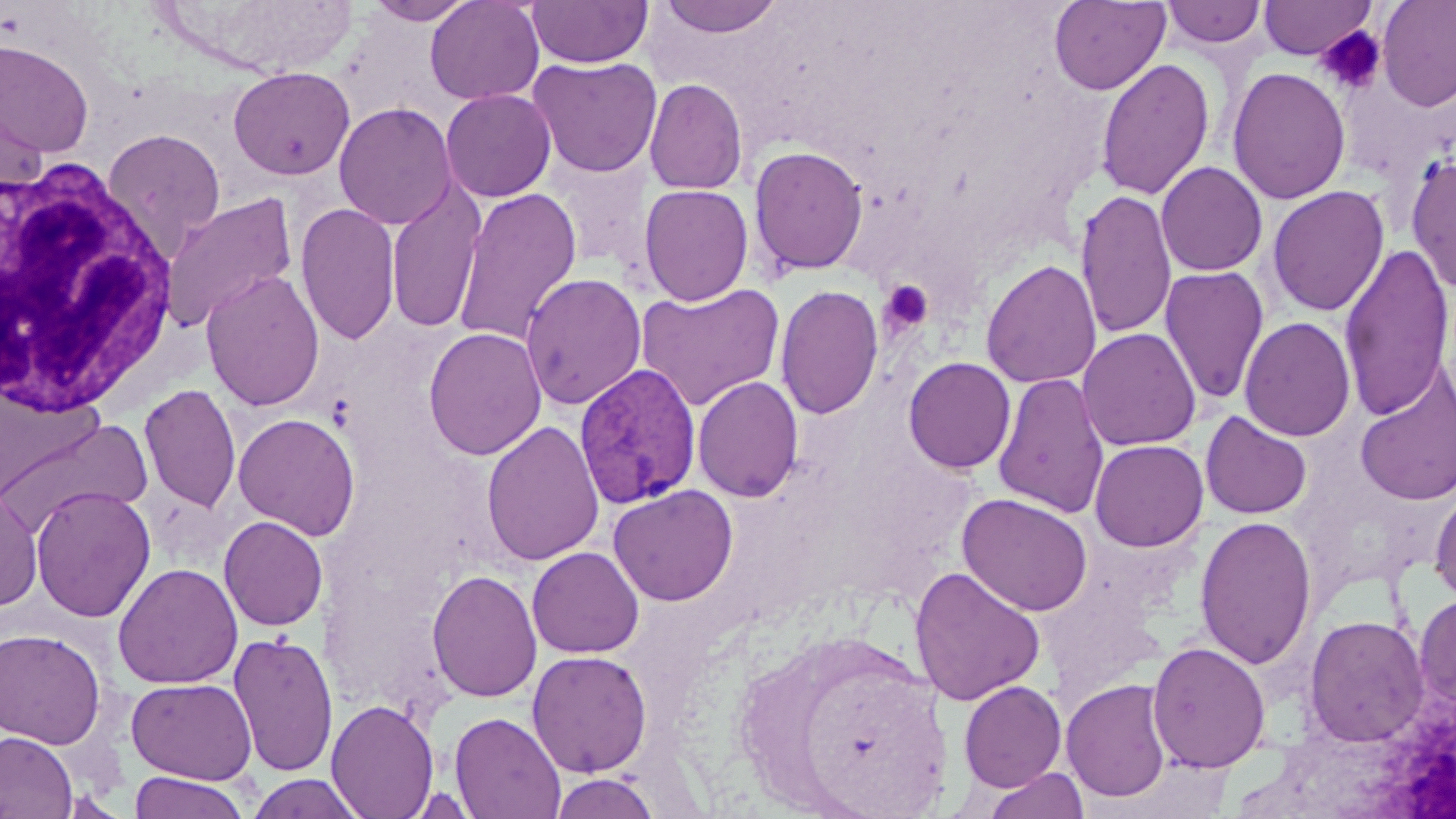
Summary:
  - Coordinate format: approximate bounding boxes as (x1,y1)-(x2,y2) corner pairs in pixels
  - Plasmodium vivax-infected red blood cell locations: (574,363)-(702,509)
  - White blood cell locations: (0,155)-(178,420)
  - Uninfected red blood cell locations: (364,0)-(478,25), (424,0)-(545,105), (527,0)-(652,68), (654,0)-(787,38), (1257,0)-(1377,60), (1377,0)-(1456,112), (1049,1)-(1170,95), (1160,1)-(1267,49), (0,38)-(95,160), (527,56)-(663,178), (1095,57)-(1215,201), (228,66)-(355,180), (1227,66)-(1351,204), (644,78)-(748,195), (0,80)-(48,199), (440,89)-(556,202), (334,102)-(456,230), (102,127)-(226,256), (748,145)-(869,276), (1406,151)-(1456,296), (547,157)-(654,269), (1156,161)-(1268,277), (386,180)-(487,335), (639,184)-(753,306), (1267,185)-(1389,317), (452,187)-(583,348), (1074,188)-(1177,342), (160,192)-(297,333), (295,202)-(401,346), (1338,242)-(1455,422), (980,258)-(1102,389), (1159,266)-(1270,405), (200,269)-(325,411), (520,273)-(647,410), (635,281)-(785,411), (775,284)-(885,420), (1239,317)-(1356,442), (423,327)-(547,460), (1078,327)-(1201,451), (902,356)-(1017,474), (1355,366)-(1455,507), (992,372)-(1110,519), (692,376)-(804,502), (139,383)-(241,513), (1200,410)-(1313,520), (233,412)-(361,541), (0,417)-(152,536), (481,420)-(604,567), (1090,439)-(1208,551), (608,484)-(738,606), (30,485)-(156,622), (1429,485)-(1456,603), (0,486)-(42,611), (956,492)-(1094,616), (218,515)-(328,632), (1194,515)-(1317,670), (527,546)-(645,658), (113,562)-(242,689), (909,565)-(1046,706), (427,568)-(542,702), (1414,591)-(1456,711), (1303,614)-(1430,747), (0,627)-(106,749), (228,631)-(339,777), (1147,640)-(1271,773), (527,650)-(653,777), (126,677)-(257,785), (1061,678)-(1172,803), (958,680)-(1067,792), (326,698)-(438,818), (449,711)-(566,819), (0,731)-(77,819), (982,768)-(1090,819), (128,770)-(251,819), (549,771)-(662,818), (246,773)-(367,819), (399,786)-(484,818)
  - Platelet locations: (1316,25)-(1386,96), (879,279)-(934,335)
  - Slide-level diagnosis: Plasmodium vivax
  - Magnification: 1000x
  - Modality: light microscopy
  - Image size: 1456×819 pixels
  - Preparation: thin blood film
  - Field of view: one of a larger specimen
  - Stain: May-Grünwald-Giemsa